Comment on the morphology of the erythrocytes.
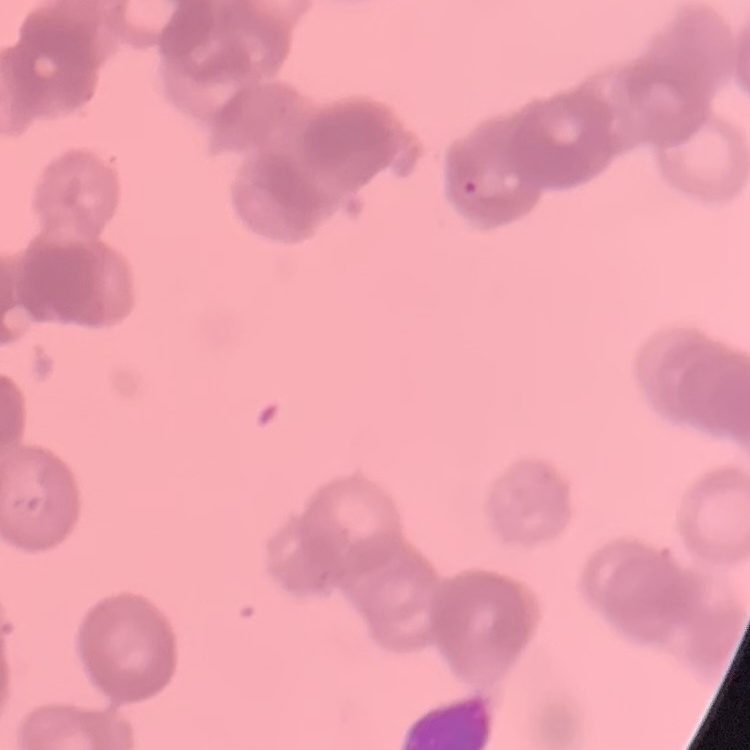
Rouleaux formation.

{
  "stain": "Field's or Giemsa",
  "preparation": "thin blood smear",
  "image_type": "square crop of a larger photomicrograph"
}